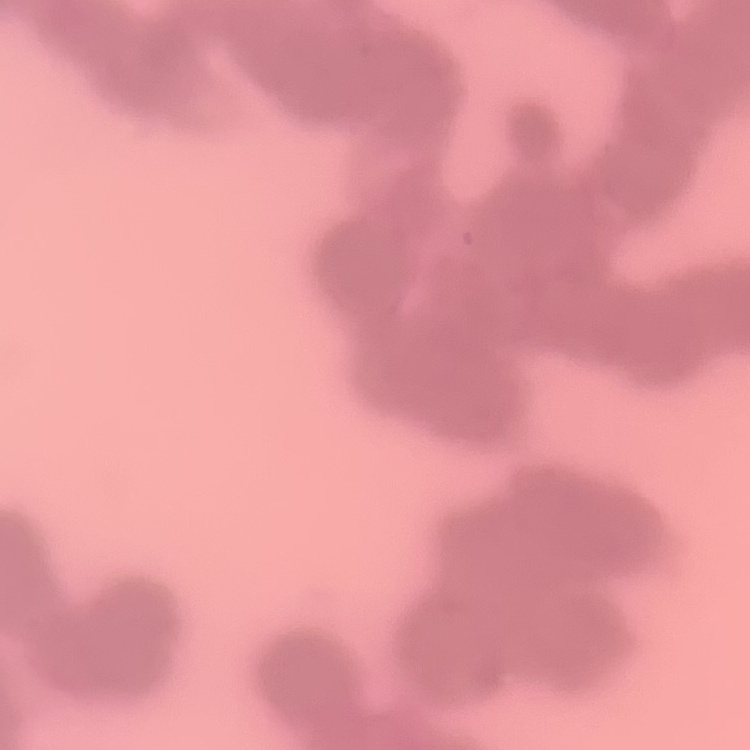
The erythrocytes show rouleaux formation. One tile cut from a larger photomicrograph. Field's or Giemsa stain. Thin peripheral smear.